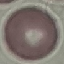

Summary:
  - Result: negative for malaria parasites
  - Image type: automatically extracted cell patch, resized to 64 × 64 pixels
  - Stain: Giemsa
  - Preparation: thin blood film
  - Capture: smartphone through the microscope eyepiece